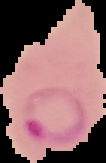
Image is 106×163 pixels. The area outside the segmented cell region is set to black. Result: malaria parasites detected. From a thin blood film.